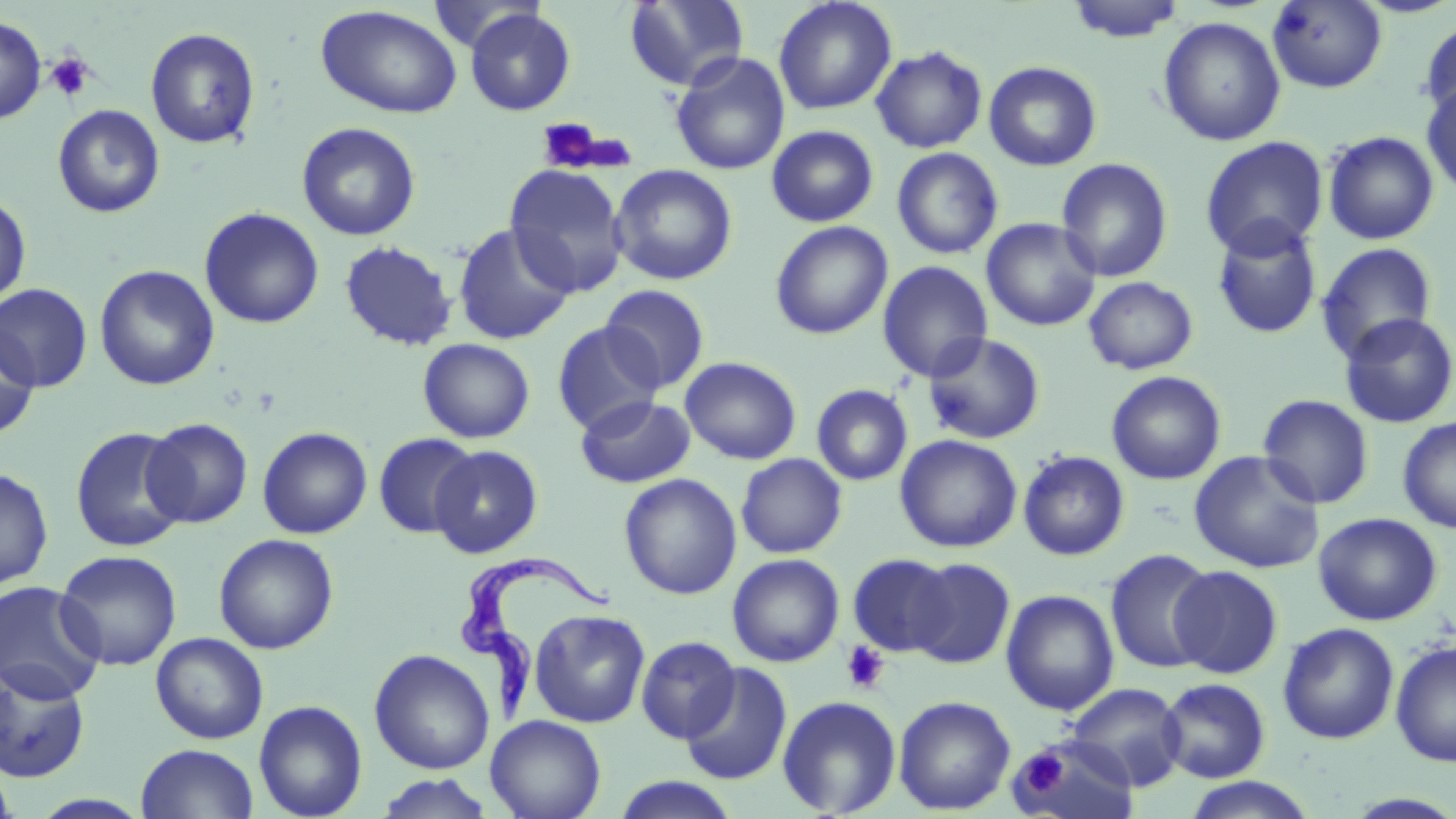

Summary:
  - Coordinate format: approximate bounding boxes as [x1, y1, x2, y2] in pixels
  - Uninfected red blood cell locations: [624, 0, 748, 91], [773, 0, 897, 115], [1064, 0, 1187, 43], [1266, 0, 1388, 94], [316, 5, 463, 119], [464, 7, 576, 116], [0, 15, 46, 124], [1158, 16, 1286, 146], [1419, 16, 1456, 122], [145, 27, 261, 149], [870, 45, 988, 153], [670, 52, 790, 176], [983, 61, 1102, 171], [1421, 80, 1456, 198], [52, 104, 165, 218], [296, 121, 422, 241], [766, 125, 879, 227], [1322, 130, 1439, 245], [1199, 136, 1329, 258], [891, 146, 1004, 260], [1056, 157, 1174, 283], [609, 163, 738, 286], [504, 164, 629, 297], [0, 191, 32, 308], [199, 207, 325, 329], [981, 217, 1102, 332], [1211, 218, 1323, 340], [770, 221, 893, 340], [452, 222, 577, 345], [339, 240, 458, 351], [1316, 242, 1438, 363], [877, 260, 994, 383], [94, 264, 219, 390], [1083, 276, 1198, 375], [0, 283, 93, 392], [600, 284, 710, 394], [1338, 312, 1456, 428], [552, 321, 664, 434], [0, 323, 39, 439], [922, 332, 1046, 445], [418, 338, 535, 443], [680, 356, 802, 465], [1106, 371, 1226, 484], [811, 384, 913, 486], [575, 394, 695, 488], [1257, 394, 1374, 509], [1397, 415, 1456, 534], [142, 417, 253, 528], [70, 426, 190, 552], [257, 426, 372, 539], [373, 432, 479, 539], [895, 434, 1022, 553], [430, 445, 543, 558], [1017, 450, 1130, 560], [1188, 450, 1325, 573], [736, 453, 847, 558], [0, 466, 54, 589], [619, 473, 742, 600], [1313, 512, 1442, 626], [213, 533, 338, 654], [1104, 548, 1218, 674], [54, 549, 182, 670], [727, 553, 844, 667], [848, 553, 958, 657], [906, 558, 1015, 668], [1169, 565, 1283, 678], [0, 580, 106, 703], [1001, 589, 1120, 716], [530, 609, 650, 728], [1278, 623, 1399, 744], [151, 632, 269, 744], [636, 636, 740, 743], [1390, 640, 1456, 766], [369, 649, 495, 774], [680, 662, 792, 786], [0, 665, 90, 782], [1158, 678, 1271, 783], [1066, 683, 1187, 790], [777, 695, 901, 817], [893, 695, 1015, 815], [254, 699, 367, 819], [486, 715, 606, 819], [1009, 736, 1141, 819], [136, 743, 259, 818], [0, 764, 18, 818], [374, 774, 496, 818], [610, 775, 741, 818], [1179, 776, 1319, 818]
  - Trypanosoma brucei locations: [457, 553, 601, 729]
  - Platelet locations: [46, 53, 95, 102], [535, 118, 610, 174], [841, 640, 890, 693], [1016, 748, 1066, 797]
  - Slide-level diagnosis: Trypanosoma brucei
  - Field of view: one of a larger specimen
  - Stain: May-Grünwald-Giemsa
  - Preparation: thin blood smear
  - Image size: 1456×819 pixels
  - Magnification: 1000x
  - Modality: light microscopy